Report the malaria status of this cell.
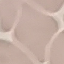
It is uninfected.

Summary:
  - Image type: automatically extracted cell patch, resized to 64 × 64 pixels
  - Stain: Giemsa
  - Capture: smartphone camera at the microscope eyepiece
  - Preparation: thin blood film